Classify this cell by malaria status.
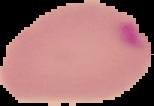
Parasitized.

Image is 154×106 pixels. From a thin blood film. The area outside the segmented cell region is set to black.